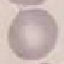

Summary:
  - Result: no malaria parasites detected
  - Capture: smartphone through the microscope eyepiece
  - Image type: automatically extracted cell patch, resized to 64 × 64 pixels
  - Stain: Giemsa
  - Preparation: thin smear